Comment on the morphology of the erythrocytes.
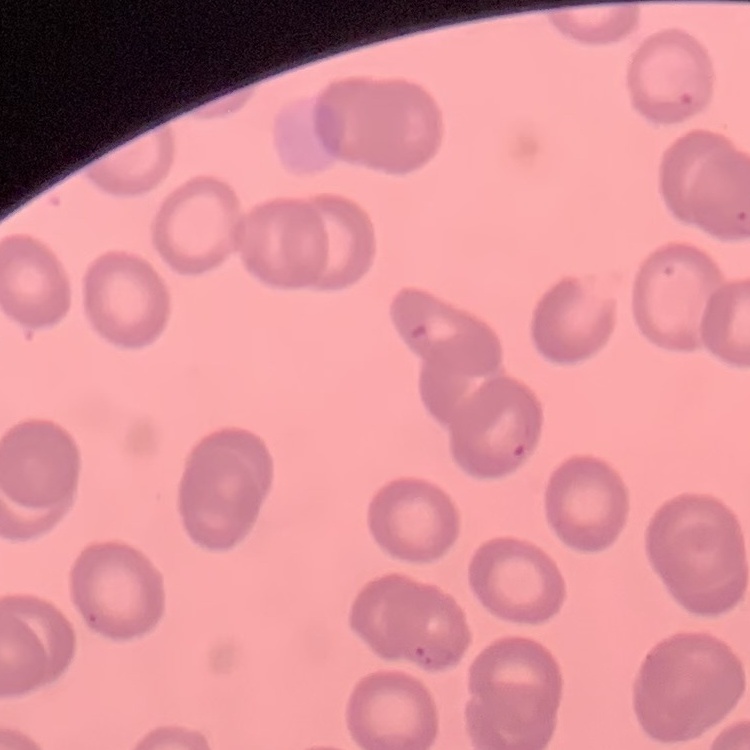

No rouleaux formation.

image type = square crop of a larger photomicrograph
preparation = thin blood film
stain = Field's or Giemsa